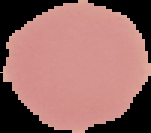
Summary:
  - Preparation: thin blood film
  - Image type: segmented cell region on a black background
  - Image size: 151×133 pixels
  - Result: negative for malaria parasites